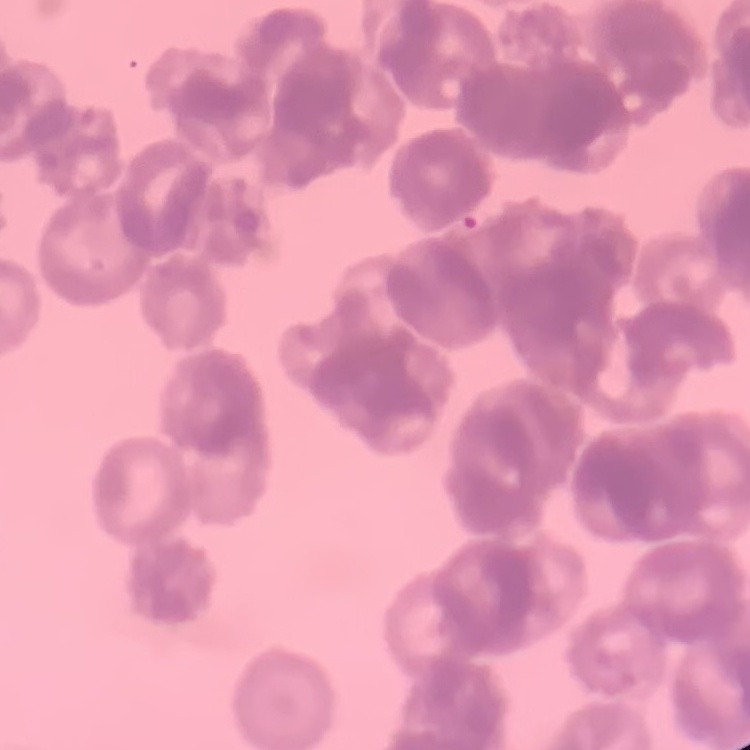

erythrocyte_morphology: rouleaux formation
stain: Field's or Giemsa
image_type: one tile cut from a larger photomicrograph
preparation: thin blood film